Outline platelets.
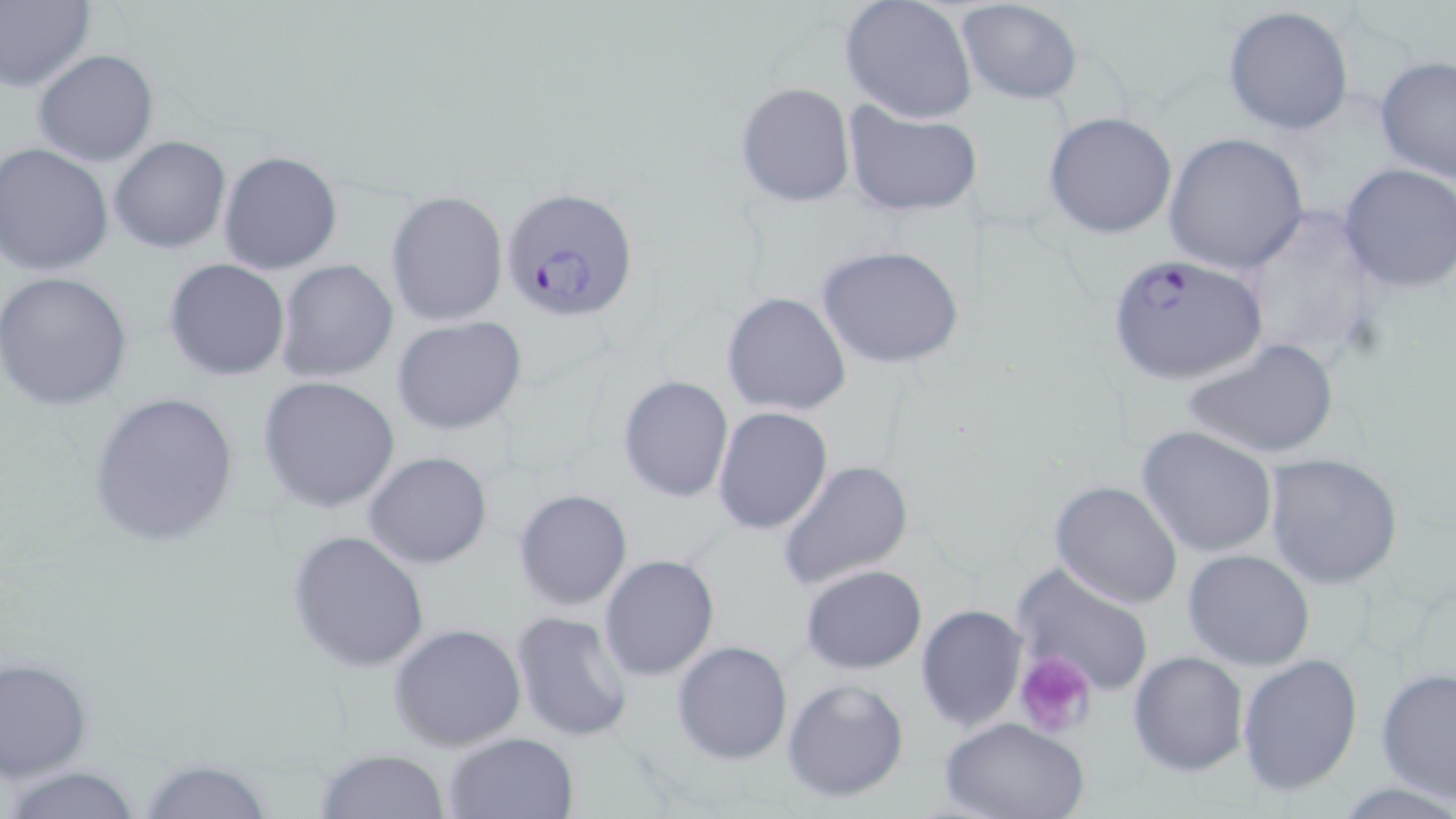
Approximate bounding boxes as (x1,y1)-(x2,y2) corner pairs in pixels.
Platelets: (1015,651)-(1097,740).

slide-level diagnosis = Plasmodium falciparum
magnification = 1000x
image size = 1456×819 pixels
Plasmodium falciparum-infected red blood cell locations = approximate bounding boxes as (x1,y1)-(x2,y2) corner pairs in pixels: (502,188)-(640,323), (1104,253)-(1268,382)
preparation = thin blood smear
field of view = one of a larger specimen
modality = light microscopy
stain = May-Grünwald-Giemsa
uninfected red blood cell locations = approximate bounding boxes as (x1,y1)-(x2,y2) corner pairs in pixels: (0,0)-(94,93), (839,0)-(978,124), (956,1)-(1086,106), (1221,5)-(1355,137), (33,50)-(158,166), (1375,57)-(1456,186), (735,81)-(856,208), (841,101)-(984,217), (1043,111)-(1178,239), (1164,132)-(1308,273), (110,136)-(231,255), (1,145)-(115,277), (218,151)-(344,275), (1337,162)-(1456,294), (386,190)-(508,326), (1234,203)-(1388,369), (817,243)-(966,370), (164,259)-(290,382), (276,260)-(399,385), (0,273)-(131,410), (722,291)-(853,418), (392,316)-(527,434), (1183,338)-(1339,461), (617,374)-(735,503), (256,376)-(400,513), (89,390)-(238,551), (711,406)-(833,535), (1135,425)-(1280,558), (363,450)-(493,569), (1263,452)-(1403,589), (777,460)-(914,590), (1050,481)-(1184,610), (513,489)-(633,610), (287,528)-(430,671), (1182,549)-(1315,669), (598,554)-(720,682), (1009,562)-(1156,696), (799,564)-(928,674), (915,605)-(1029,732), (509,610)-(634,741), (389,623)-(528,751), (671,640)-(793,765), (1128,650)-(1250,777), (1238,654)-(1364,794), (0,658)-(90,781), (1377,667)-(1456,803), (782,677)-(910,803), (939,715)-(1089,819), (442,730)-(580,819), (315,747)-(451,819), (137,759)-(276,818), (7,765)-(145,819)